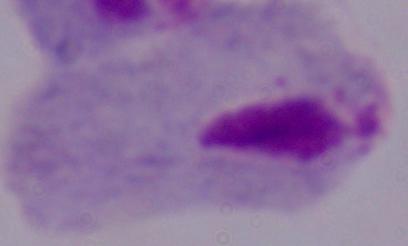

identification: trichomonad
magnification: 1000x
modality: micrograph